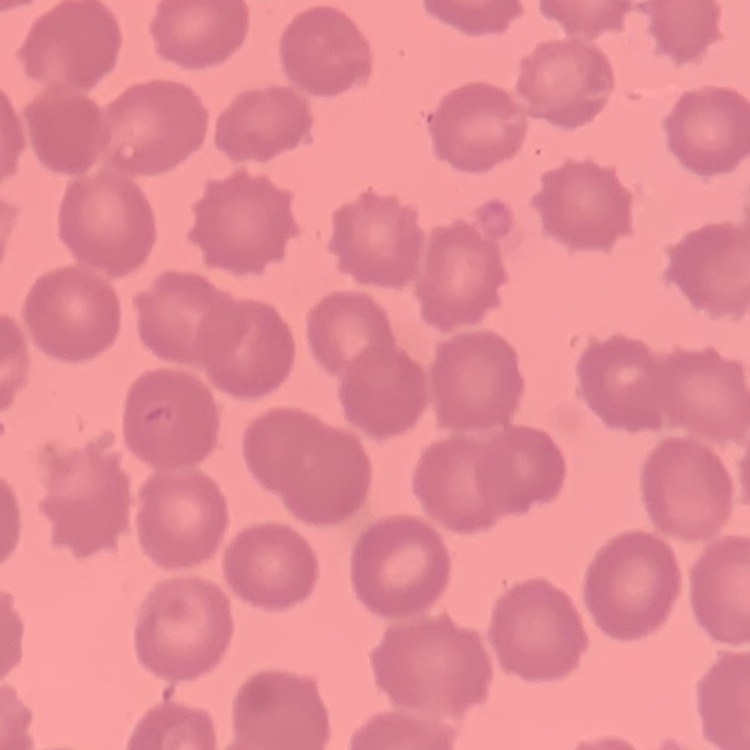

The erythrocytes show no rouleaux formation. Square crop of a larger photomicrograph. Stained with either Field's or Giemsa. Thin peripheral smear.